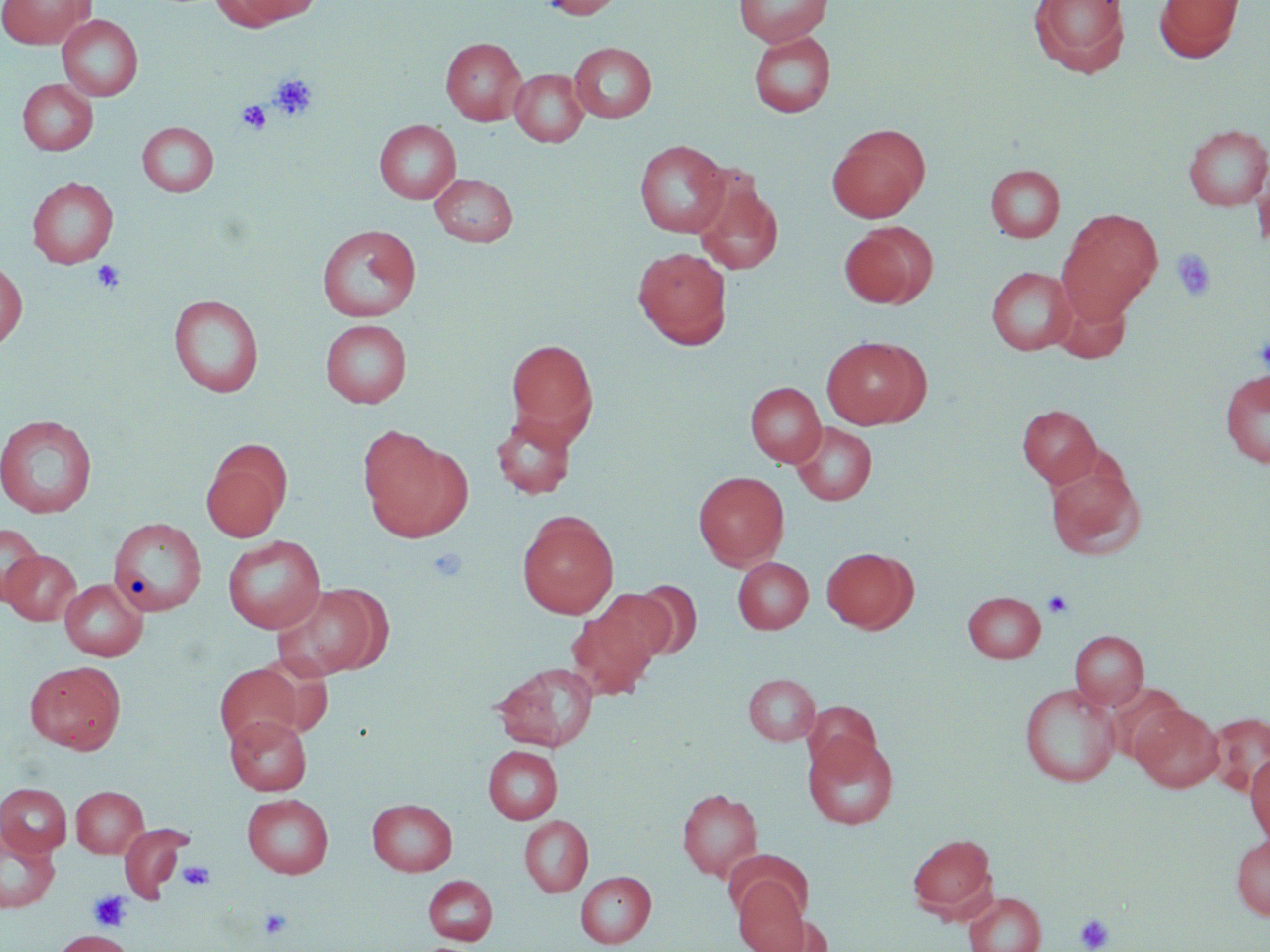
Summary:
  - Coordinate format: approximate bounding boxes as [x1, y1, x2, y2] in pixels
  - Uninfected red blood cell locations (subset): [0, 0, 95, 49], [210, 0, 317, 29], [538, 0, 627, 19], [733, 0, 833, 46], [1028, 0, 1130, 77], [1154, 0, 1244, 62], [57, 14, 143, 101], [748, 31, 836, 118], [440, 37, 527, 125], [569, 42, 657, 122], [509, 68, 588, 147], [17, 79, 98, 155], [374, 120, 462, 204], [137, 122, 219, 197], [1182, 124, 1270, 210], [827, 125, 930, 222], [634, 139, 731, 237], [1251, 162, 1269, 254], [985, 165, 1065, 242], [691, 171, 784, 276], [429, 173, 518, 246], [27, 177, 118, 268], [1056, 209, 1162, 321], [839, 223, 937, 309], [317, 224, 421, 322], [633, 246, 732, 349], [0, 259, 28, 350], [986, 266, 1077, 355], [1049, 288, 1132, 364], [169, 294, 264, 398], [321, 319, 412, 407], [821, 335, 930, 429], [505, 338, 598, 441], [1219, 369, 1270, 469], [745, 381, 826, 467], [1017, 404, 1102, 487], [490, 412, 577, 499], [0, 414, 97, 518], [791, 422, 876, 506], [358, 430, 472, 542], [201, 440, 292, 541], [1045, 460, 1146, 560], [693, 471, 789, 568], [517, 511, 619, 619], [108, 517, 207, 617], [0, 522, 45, 606], [222, 534, 326, 633], [821, 546, 917, 633], [2, 549, 82, 625], [732, 556, 813, 634], [60, 579, 148, 660], [628, 579, 702, 660], [275, 583, 389, 679], [593, 589, 678, 667], [963, 591, 1046, 662], [566, 604, 660, 699], [1070, 630, 1148, 710], [25, 660, 126, 754], [493, 662, 599, 751], [214, 663, 306, 749], [743, 673, 820, 745], [1019, 683, 1120, 787], [802, 701, 881, 778], [1131, 703, 1224, 792], [1206, 712, 1270, 796], [225, 714, 311, 795], [803, 732, 899, 830], [483, 745, 562, 824], [1245, 752, 1270, 846], [0, 783, 72, 856], [71, 786, 148, 858], [676, 787, 763, 880], [242, 793, 334, 878], [367, 798, 457, 875], [519, 816, 593, 896], [0, 826, 60, 913], [907, 833, 996, 919], [1231, 835, 1270, 921], [575, 870, 656, 948], [423, 875, 498, 945], [733, 876, 809, 952], [963, 892, 1046, 952], [753, 914, 832, 951], [51, 929, 135, 952]
  - Platelet locations (subset): [270, 73, 318, 122], [237, 100, 272, 135], [1171, 249, 1217, 302], [92, 259, 126, 294], [1255, 333, 1270, 374], [428, 546, 468, 582], [1043, 590, 1073, 618], [178, 861, 215, 890], [89, 890, 132, 932], [259, 907, 292, 939], [1075, 913, 1114, 952]
  - Slide-level diagnosis: no evidence of blood parasites
  - Image size: 1270×952 pixels
  - Modality: light microscopy
  - Magnification: 1000x
  - Field of view: single
  - Preparation: thin blood film
  - Stain: May-Grünwald-Giemsa